Describe the morphology of the red blood cells.
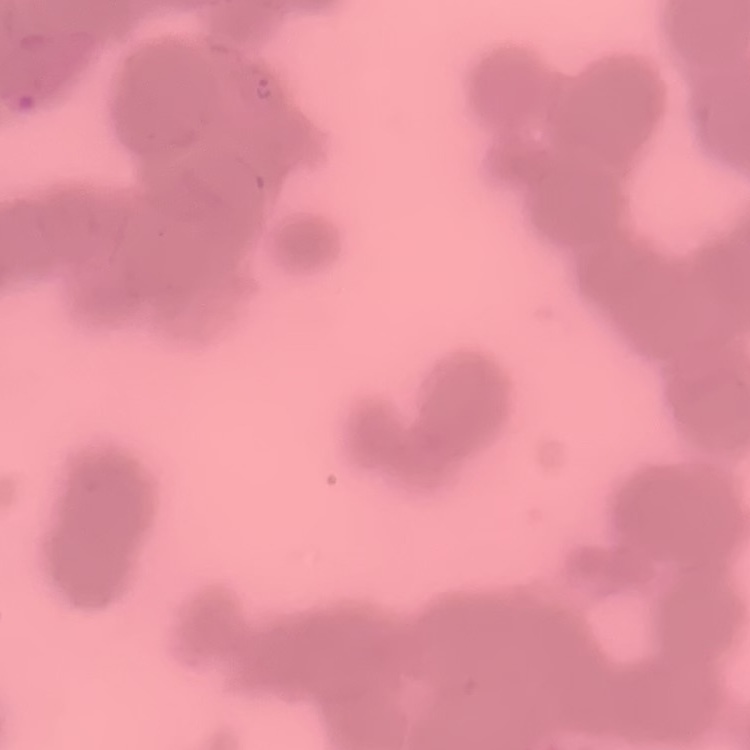
Rouleaux formation.

One tile cut from a larger photomicrograph. Thin blood smear. Stained with either Field's or Giemsa.